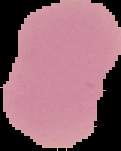

Summary:
  - Preparation: thin blood film
  - Result: no Plasmodium parasites detected
  - Image type: segmented cell region with the area outside set to black
  - Image size: 121×151 pixels